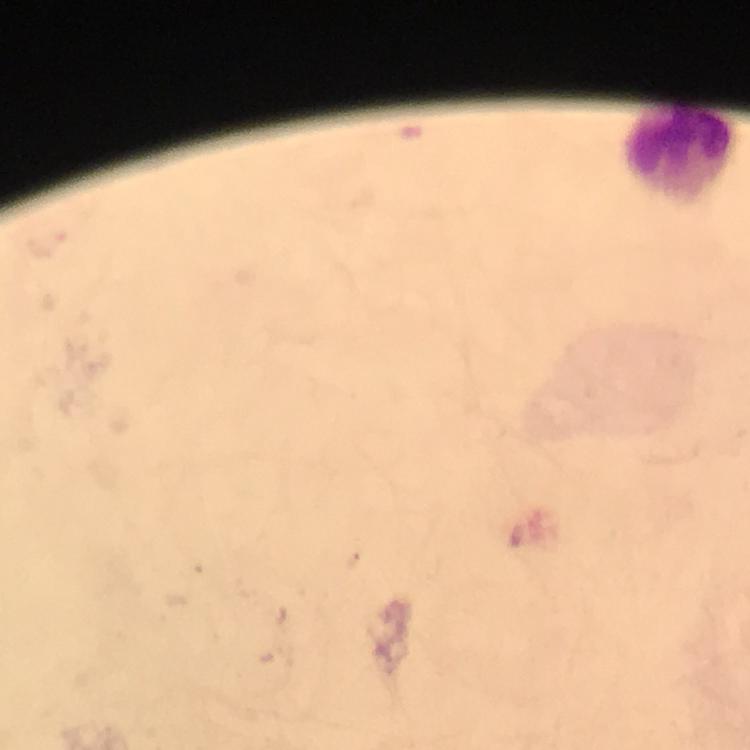
preparation = thick blood smear
Plasmodium parasites = none seen
image size = 750×750 pixels
context = from a malaria diagnostic workup
immersion oil = applied
cropped from = a single field of view
leukocyte locations = approximate centers as [x, y] in pixels: [679, 154]
capture = smartphone camera through the microscope
stain = Giemsa
magnification = 100x